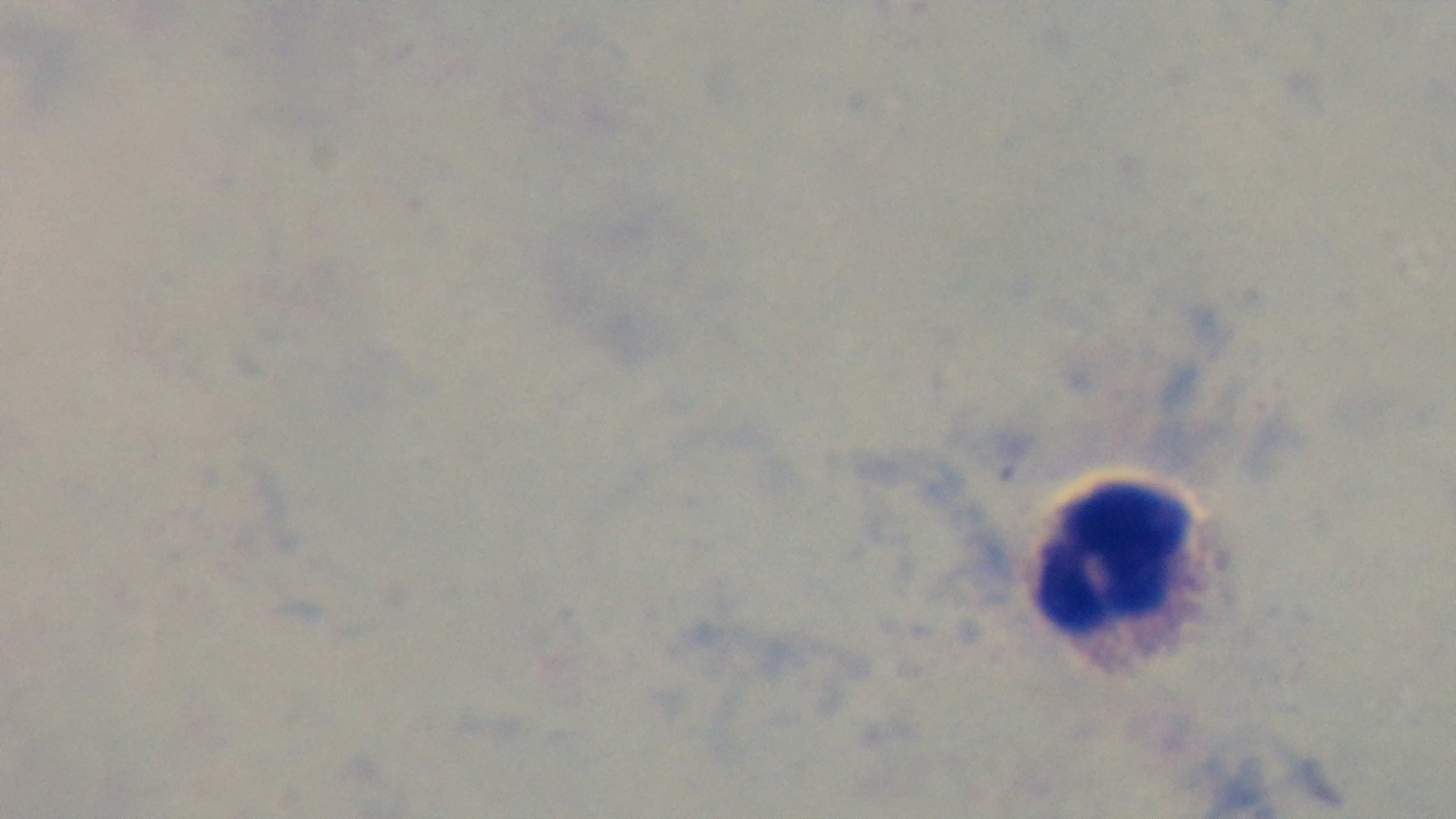
stain = Giemsa
preparation = thick smear
modality = light microscopy
objective = 100x oil immersion
malaria status = uninfected
field of view = one from the slide
capture = mounted 4K digital camera